Assess for Plasmodium parasites.
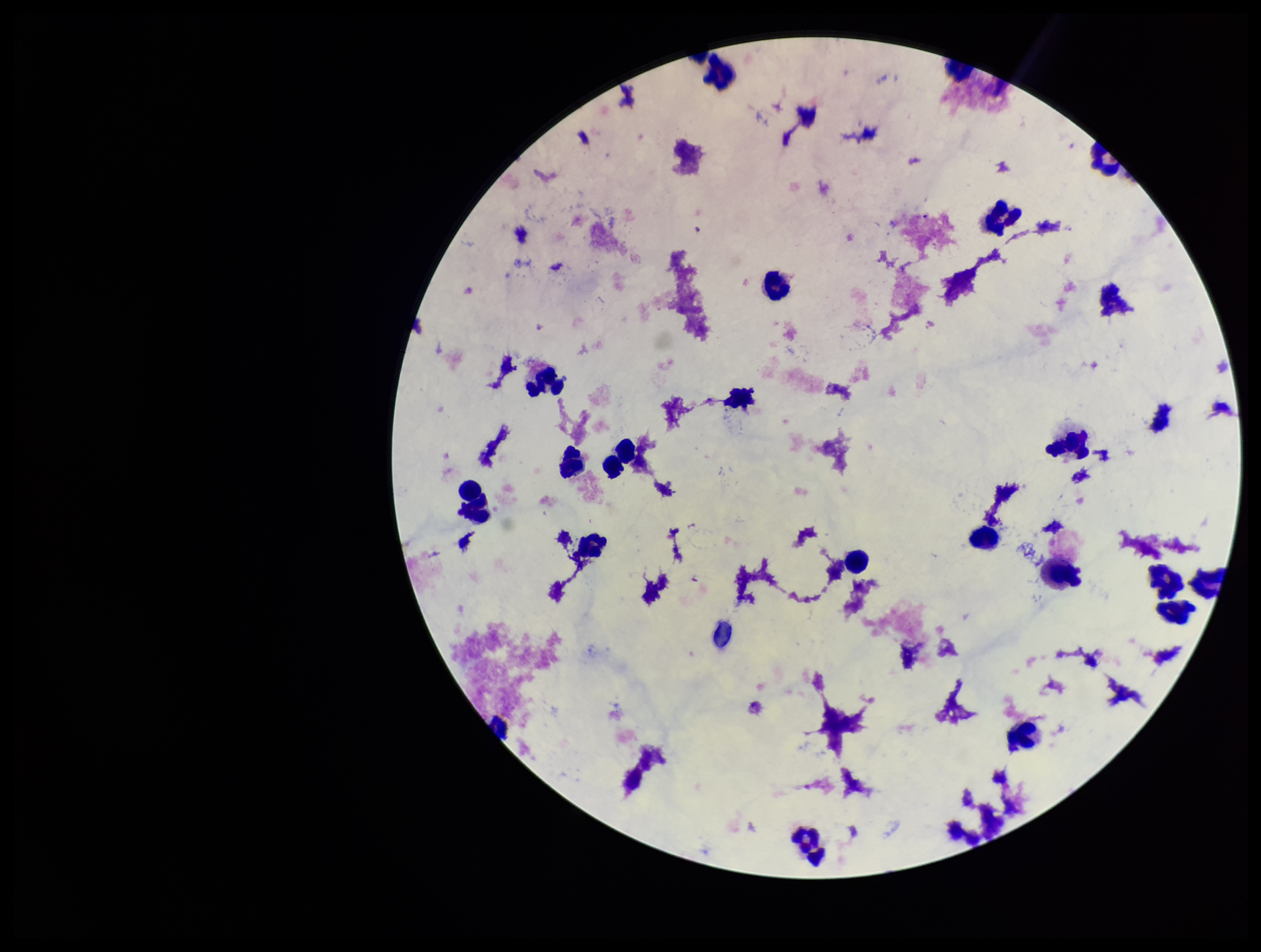
None seen.

Stained with Giemsa. Leukocyte count: 21. Patient malaria status: negative. Image is 1261×952 pixels. Preparation: thick blood smear. One field from this slide. Photographed through the microscope eyepiece with a smartphone camera. Parasite count: 0.